Identify the parasite.
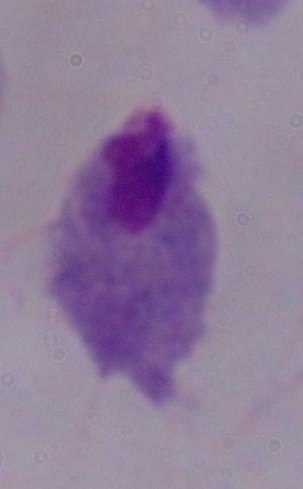
This is a trichomonad.

Summary:
  - Magnification: 1000x
  - Modality: photomicrograph